Describe the morphology of the erythrocytes.
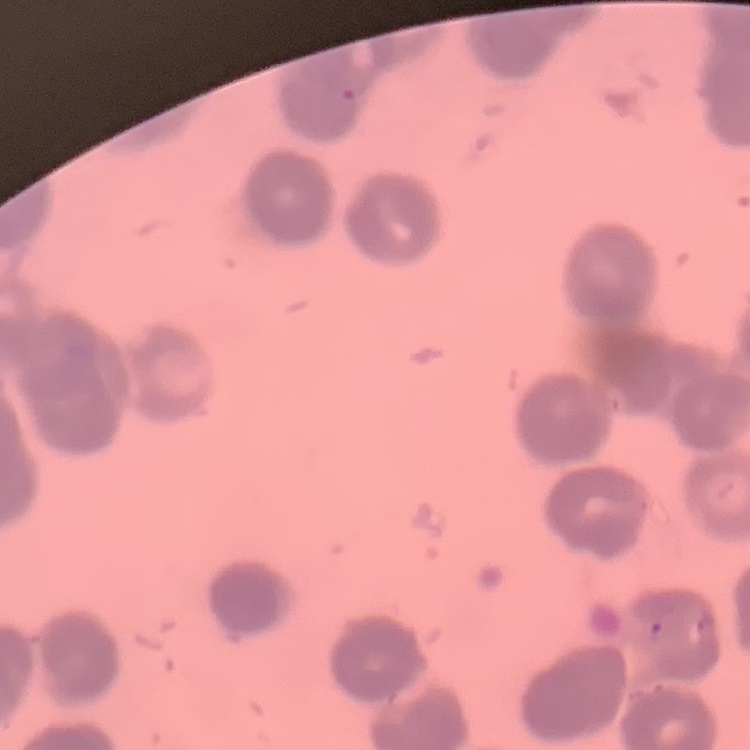

Rouleaux formation.

stain: Field's or Giemsa
preparation: thin blood film
image_type: one tile cut from a larger photomicrograph